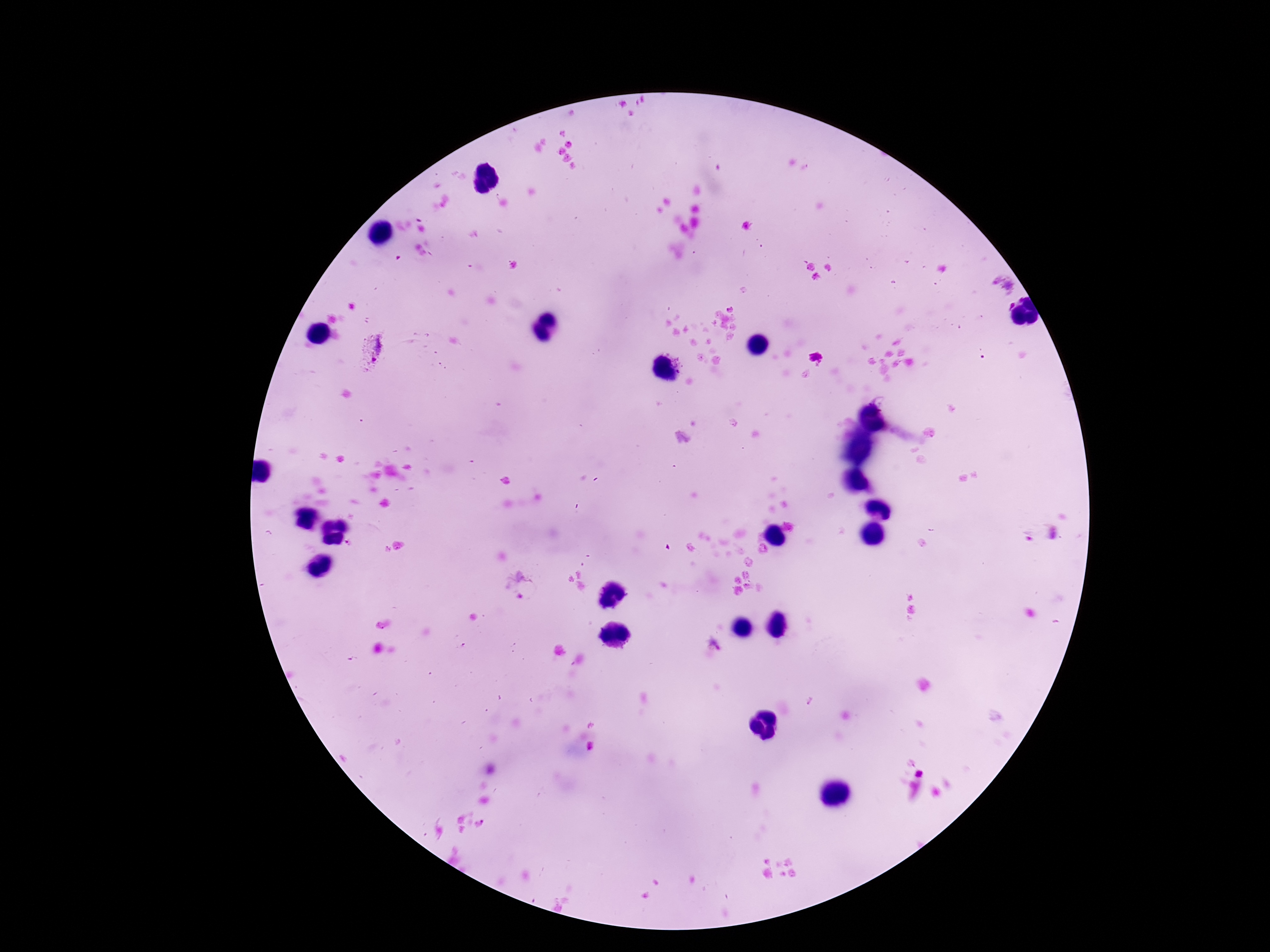
Approximate centers as (x, y) in pixels.
Summary:
  - Plasmodium parasite locations: (1002, 287), (373, 349), (714, 646), (480, 823)
  - Stain: Giemsa
  - Preparation: thick blood film
  - Field of view: one from this slide
  - Capture: smartphone camera through the microscope eyepiece
  - Magnification: 100x
  - Patient malaria status: infected
  - Image size: 1270×952 pixels